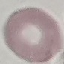

malaria status = uninfected
preparation = thin blood film
stain = Giemsa
image type = cell patch, automatically extracted from a larger field of view and resized to 64 × 64 pixels
capture = smartphone through the microscope eyepiece